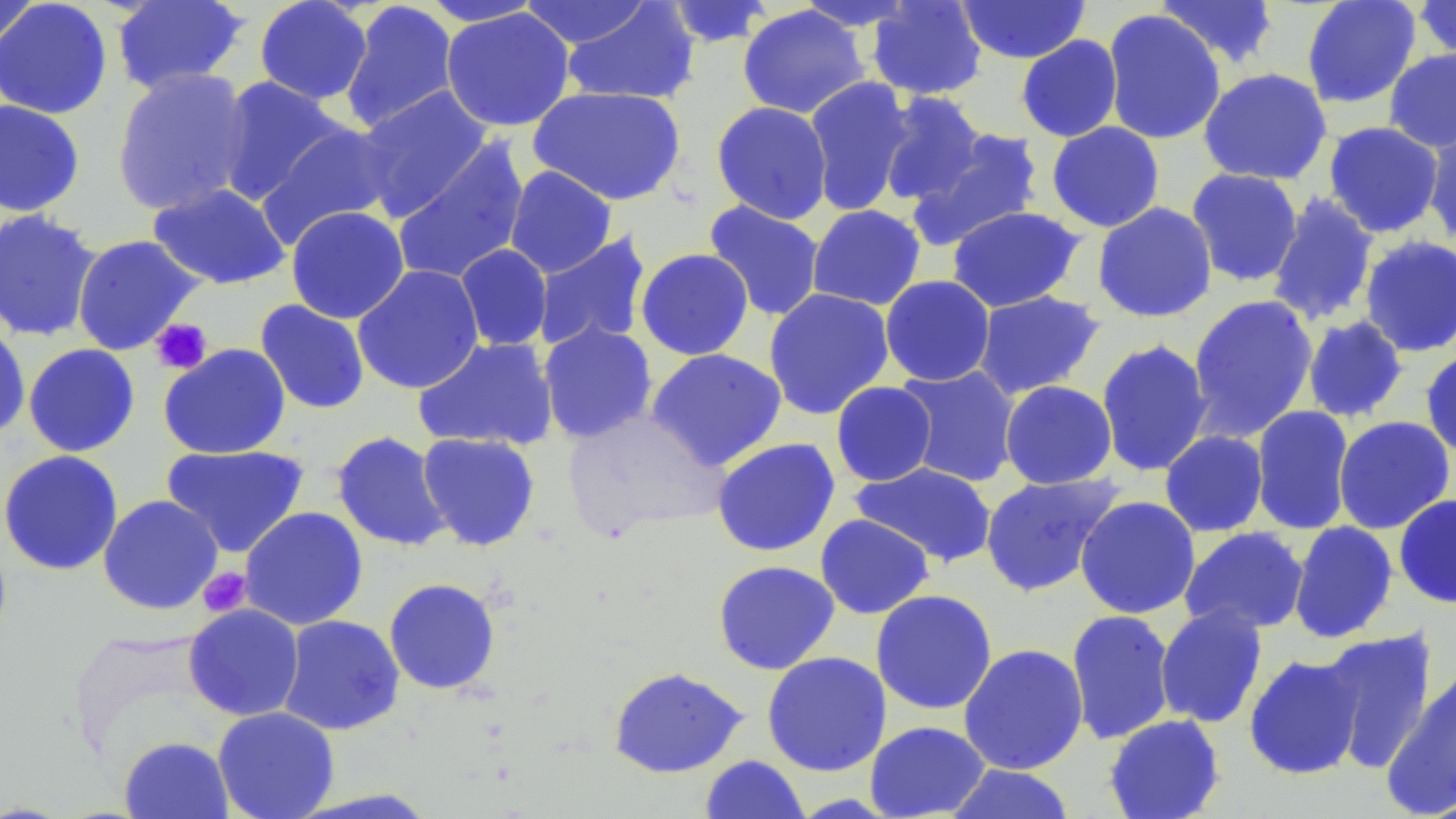
{
  "slide_level_diagnosis": "negative for blood parasites",
  "modality": "optical microscopy",
  "image_size": "1456×819 pixels",
  "magnification": "1000x",
  "platelet_locations": "approximate bounding boxes as (x1,y1)-(x2,y2) corner pairs in pixels: (150,318)-(212,374), (198,567)-(253,617)",
  "preparation": "thin blood film",
  "stain": "May-Grünwald-Giemsa",
  "uninfected_red_blood_cell_locations": "approximate bounding boxes as (x1,y1)-(x2,y2) corner pairs in pixels: (0,0)-(40,60), (110,0)-(249,96), (253,0)-(374,105), (417,0)-(547,27), (519,0)-(655,50), (795,0)-(919,31), (866,0)-(988,100), (1152,0)-(1281,69), (1301,0)-(1421,109), (1412,0)-(1456,65), (0,1)-(113,119), (340,1)-(460,134), (561,1)-(700,105), (661,1)-(776,48), (956,1)-(1091,64), (737,4)-(871,119), (440,7)-(576,132), (1101,10)-(1226,145), (1016,34)-(1123,142), (1384,48)-(1456,153), (111,67)-(254,216), (1198,67)-(1332,186), (215,76)-(349,207), (804,76)-(915,216), (527,85)-(687,206), (354,86)-(493,222), (876,92)-(988,205), (0,100)-(85,217), (711,101)-(833,224), (1046,121)-(1165,233), (1322,121)-(1445,238), (258,122)-(397,246), (1421,123)-(1456,247), (907,129)-(1045,250), (391,139)-(529,285), (504,165)-(617,278), (1186,168)-(1304,287), (147,182)-(290,290), (1266,192)-(1380,327), (703,200)-(825,322), (1092,202)-(1218,323), (808,204)-(926,310), (947,205)-(1084,312), (286,206)-(410,324), (0,208)-(102,343), (532,232)-(652,352), (71,234)-(203,355), (1359,235)-(1456,357), (455,244)-(552,351), (635,248)-(754,360), (352,265)-(485,395), (880,275)-(995,386), (763,288)-(895,420), (972,290)-(1106,399), (1186,294)-(1319,441), (254,299)-(370,415), (1301,315)-(1409,423), (0,317)-(31,440), (538,322)-(657,443), (412,336)-(559,451), (1096,338)-(1214,477), (23,343)-(140,457), (158,343)-(291,460), (646,348)-(788,471), (1420,348)-(1456,459), (894,365)-(1021,487), (999,380)-(1118,489), (831,381)-(937,486), (1250,405)-(1355,534), (562,408)-(728,540), (1333,416)-(1455,534), (331,430)-(451,552), (1159,430)-(1269,537), (417,432)-(542,551), (711,437)-(840,557), (161,444)-(310,558), (0,450)-(124,576), (850,461)-(998,568), (979,472)-(1124,598), (98,494)-(224,615), (1393,494)-(1456,608), (1075,495)-(1201,619), (239,506)-(368,630), (815,514)-(934,619), (1288,521)-(1399,643), (1179,526)-(1309,635), (712,560)-(840,675), (384,577)-(501,695), (870,589)-(998,715), (183,603)-(305,721), (1154,604)-(1268,728), (1065,609)-(1176,745), (277,614)-(405,735), (1317,627)-(1439,773), (958,643)-(1089,775), (761,651)-(892,777), (1243,653)-(1365,780), (608,666)-(748,778), (1380,667)-(1455,816), (212,706)-(340,819), (1103,713)-(1225,819), (864,720)-(991,819), (119,736)-(233,819), (699,755)-(810,818), (943,763)-(1076,819)",
  "field_of_view": "single"
}